Outline each blood parasite and name the species.
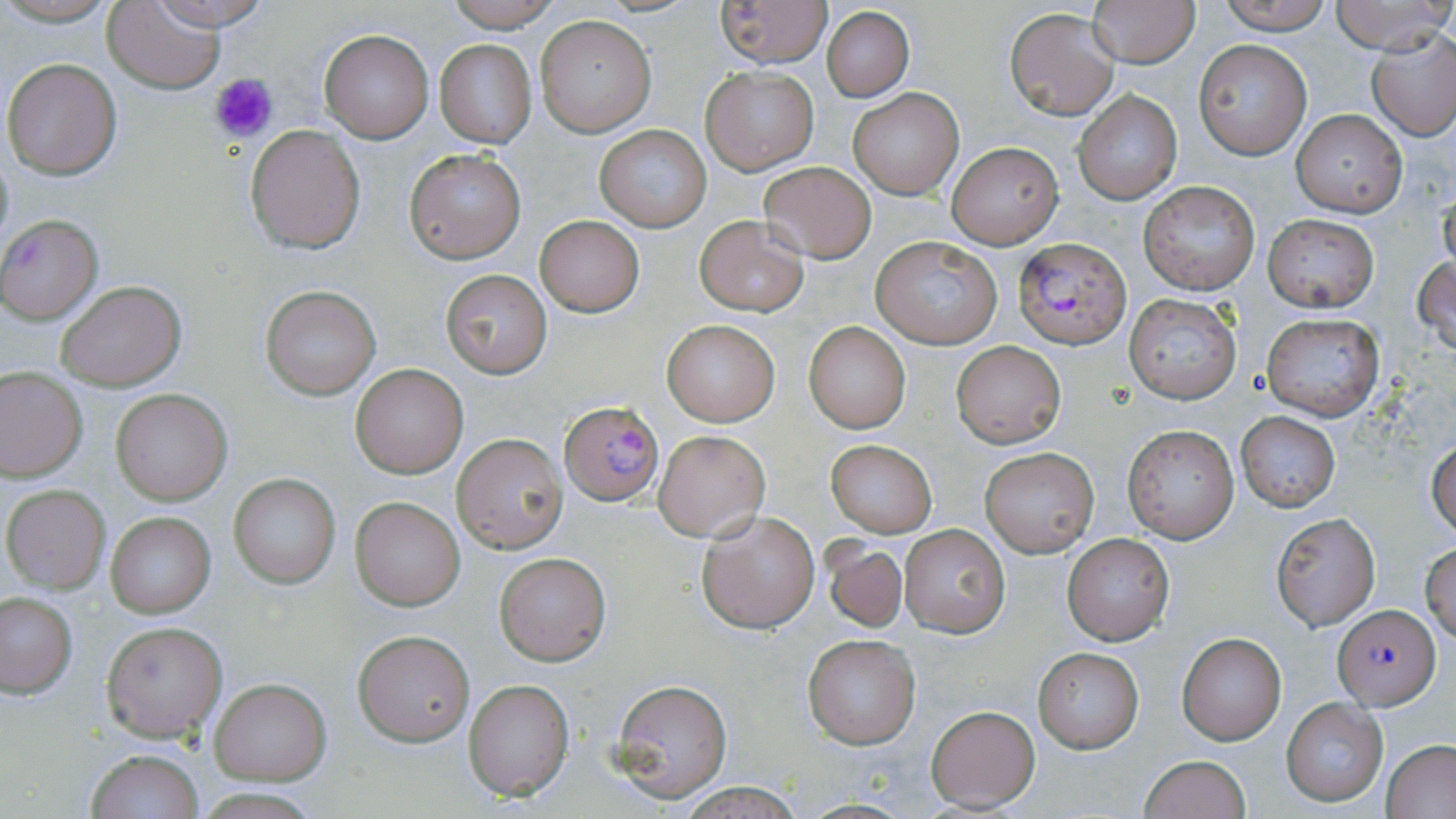
Approximate bounding boxes as (x1,y1)-(x2,y2) corner pairs in pixels.
Plasmodium falciparum-infected red blood cells: (0,215)-(104,324), (1014,236)-(1131,347), (559,399)-(665,507), (1334,606)-(1440,709).
No Plasmodium ovale, Plasmodium malariae, Plasmodium vivax, Babesia divergens, or Trypanosoma brucei observed.

Platelet locations: (209,72)-(279,143). Uninfected red blood cell locations: (0,0)-(123,26), (441,0)-(562,30), (713,0)-(832,68), (1087,0)-(1199,67), (1218,0)-(1334,35), (1328,0)-(1456,55), (102,2)-(225,91), (137,2)-(279,31), (822,6)-(915,102), (1005,9)-(1119,121), (535,16)-(655,136), (319,29)-(434,143), (1368,31)-(1456,139), (433,38)-(537,149), (1193,39)-(1312,159), (2,57)-(123,180), (701,65)-(819,174), (847,87)-(963,199), (1074,90)-(1182,205), (1292,109)-(1406,217), (594,123)-(711,232), (245,124)-(365,254), (945,141)-(1064,248), (404,148)-(526,263), (759,163)-(878,263), (711,177)-(869,296), (1137,181)-(1261,297), (1438,185)-(1456,282), (534,215)-(645,317), (1262,215)-(1379,311), (693,216)-(808,315), (870,236)-(1001,347), (1412,254)-(1456,357), (440,269)-(552,378), (55,280)-(186,391), (260,286)-(380,398), (1123,293)-(1243,405), (1260,312)-(1385,420), (662,320)-(779,425), (804,322)-(911,432), (952,341)-(1065,447), (349,362)-(469,479), (0,366)-(87,482), (110,389)-(232,505), (1235,412)-(1340,511), (1122,425)-(1238,542), (653,429)-(769,541), (451,433)-(567,553), (825,439)-(937,537), (1427,439)-(1456,538), (980,447)-(1097,556), (228,474)-(340,588), (2,484)-(110,594), (350,497)-(465,610), (697,509)-(821,631), (104,510)-(216,619), (1271,513)-(1380,632), (898,524)-(1011,638), (1062,533)-(1175,645), (822,540)-(908,633), (1421,545)-(1456,642), (494,552)-(610,665), (0,593)-(77,697), (101,620)-(227,742), (353,629)-(473,745), (1176,632)-(1287,745), (802,635)-(922,749), (1032,647)-(1144,752), (210,678)-(329,784), (610,678)-(733,802), (462,679)-(574,801), (1281,697)-(1388,806), (926,705)-(1039,812), (1381,740)-(1456,819), (84,749)-(204,819), (1139,754)-(1250,819), (673,783)-(804,817), (194,786)-(323,817). Slide-level diagnosis: Plasmodium falciparum. 1000x magnification. Image is 1456×819 pixels. May-Grünwald-Giemsa-stained preparation. Thin blood film. Light microscopy. Single field of view.